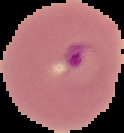

Summary:
  - Preparation: thin blood smear
  - Image size: 124×133 pixels
  - Image type: segmented cell region on a black background
  - Result: Plasmodium parasites detected